Classify this cell by malaria status.
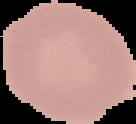
It is uninfected.

image type = segmented cell region on a black background
image size = 136×124 pixels
preparation = thin blood smear